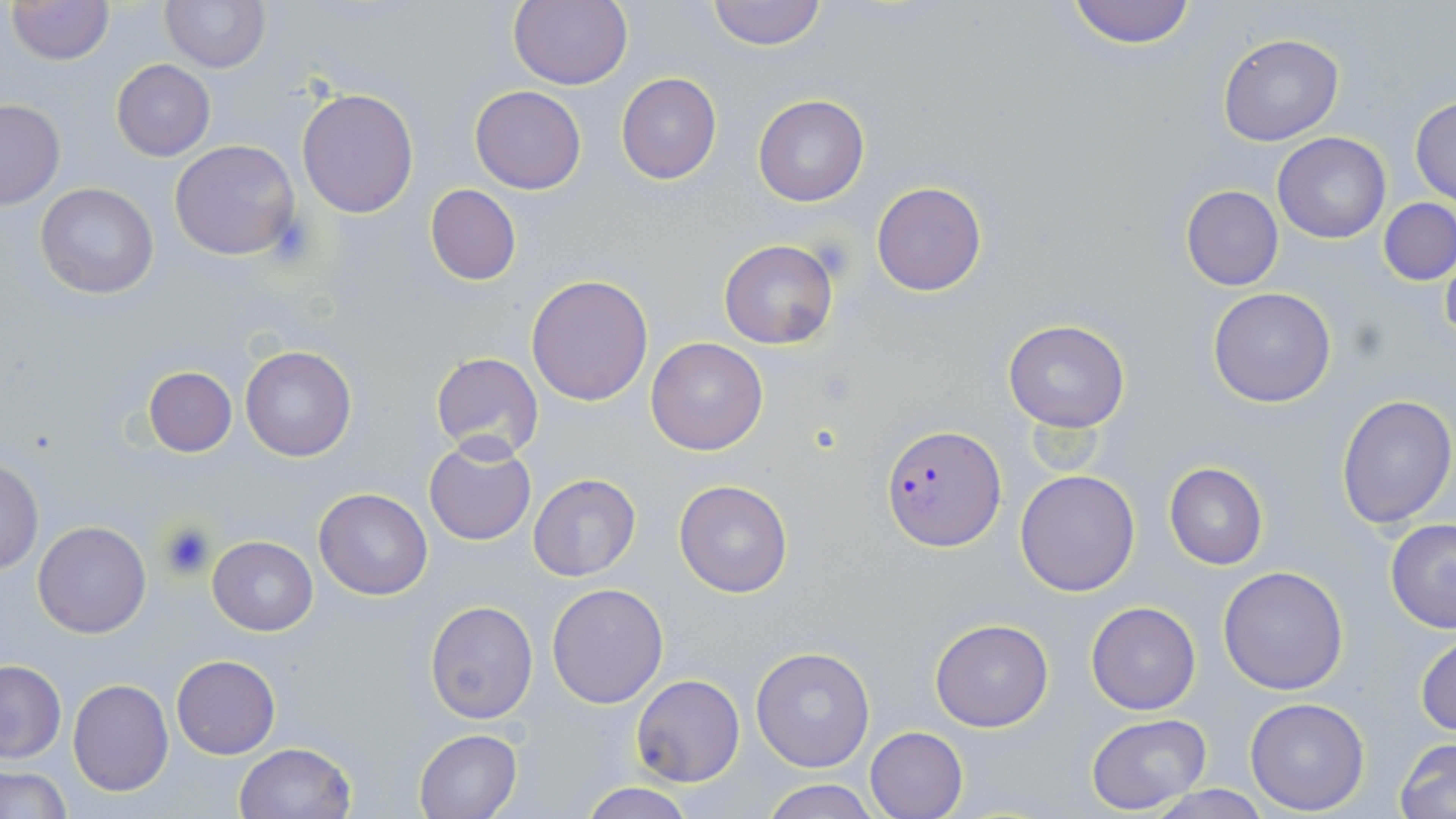
slide_level_diagnosis: Plasmodium falciparum
modality: optical microscopy
preparation: thin blood smear
magnification: 1000x
stain: May-Grünwald-Giemsa
uninfected_red_blood_cell_locations: 'approximate bounding boxes as (x1,y1)-(x2,y2) corner pairs in pixels: (7,0)-(112,65), (159,0)-(269,72), (509,0)-(633,90), (705,0)-(827,49), (1065,0)-(1200,47), (1217,32)-(1343,146), (110,60)-(216,161), (616,72)-(722,185), (470,84)-(586,194), (297,87)-(419,217), (752,94)-(870,207), (1410,96)-(1456,204), (0,98)-(64,209), (1272,132)-(1391,243), (170,139)-(300,260), (871,181)-(988,297), (35,182)-(159,299), (426,184)-(522,286), (1180,185)-(1284,291), (1380,199)-(1456,285), (718,239)-(838,349), (1440,239)-(1456,348), (526,274)-(653,406), (1207,287)-(1337,408), (1003,320)-(1130,433), (645,337)-(768,456), (240,346)-(356,462), (429,353)-(545,459), (143,365)-(237,456), (1335,393)-(1456,528), (424,438)-(536,546), (1,458)-(43,574), (1164,463)-(1268,569), (1015,469)-(1141,596), (528,473)-(641,583), (673,479)-(793,599), (314,487)-(433,600), (1384,519)-(1456,634), (32,521)-(152,637), (208,536)-(317,635), (1217,565)-(1349,695), (547,582)-(669,707), (424,599)-(540,723), (1086,601)-(1200,714), (929,618)-(1054,733), (1414,629)-(1456,738), (749,645)-(875,773), (171,654)-(280,759), (0,659)-(65,764), (630,674)-(744,788), (67,679)-(174,797), (1243,697)-(1370,815), (1087,713)-(1212,815), (864,726)-(968,819), (414,729)-(522,818), (1395,737)-(1456,818), (232,742)-(356,819), (1,767)-(71,818), (760,778)-(878,819), (578,781)-(697,819), (1146,788)-(1271,819)'
plasmodium_falciparum_infected_red_blood_cell_locations: 'approximate bounding boxes as (x1,y1)-(x2,y2) corner pairs in pixels: (881,425)-(1006,552)'
field_of_view: one of a larger specimen
image_size: 1456×819 pixels
platelet_locations: 'approximate bounding boxes as (x1,y1)-(x2,y2) corner pairs in pixels: (156,520)-(215,580)'